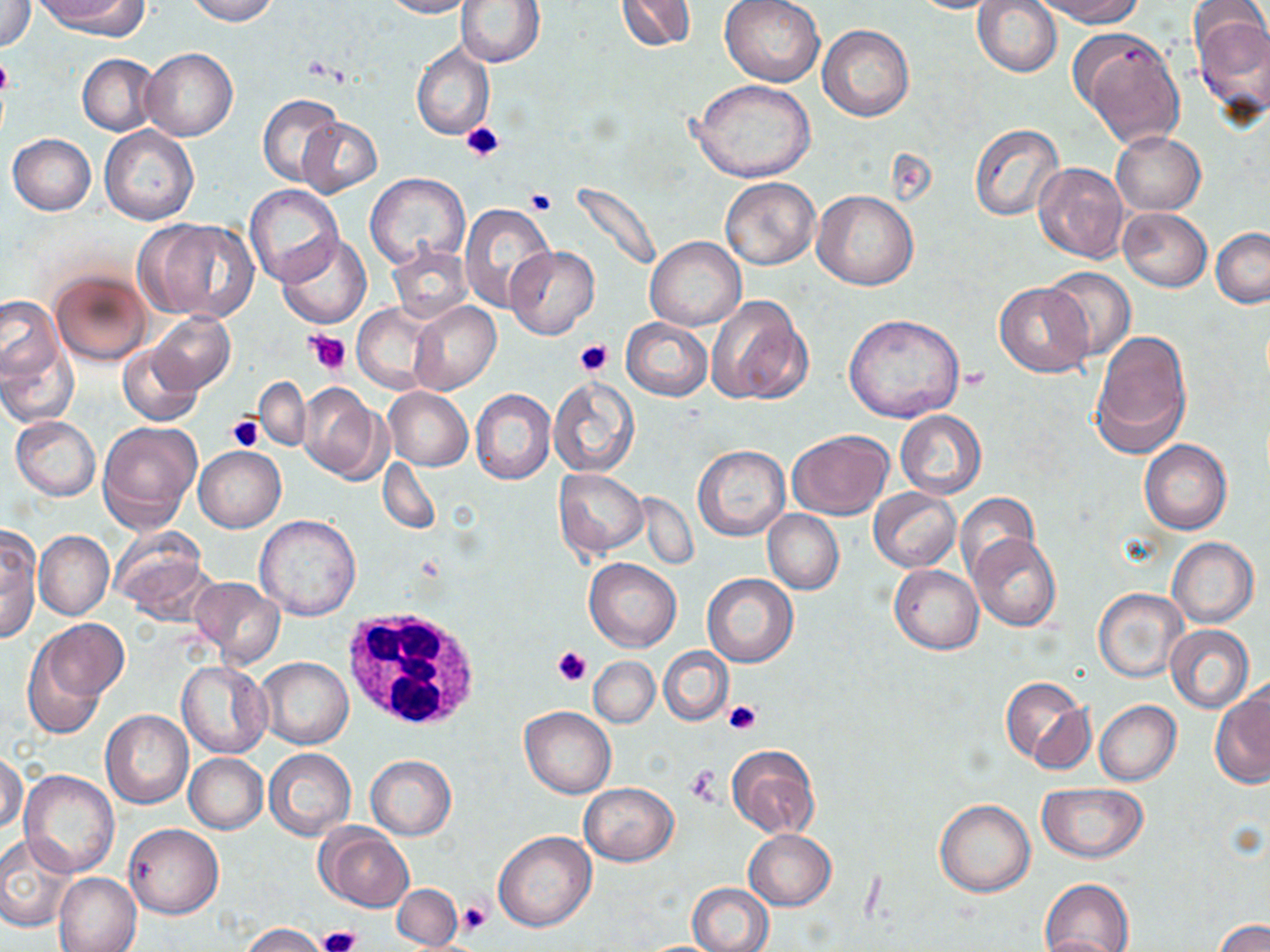 Approximate bounding boxes as [x1, y1, x2, y2] in pixels. Platelet locations: [0, 54, 14, 97], [460, 119, 504, 163], [525, 188, 556, 215], [305, 329, 351, 375], [576, 340, 614, 375], [226, 413, 263, 451], [553, 644, 591, 685], [724, 699, 762, 735], [686, 767, 722, 804], [457, 900, 492, 937], [317, 925, 362, 952]. Uninfected red blood cell locations: [38, 0, 145, 36], [184, 0, 279, 24], [380, 0, 472, 18], [456, 0, 546, 68], [613, 0, 698, 54], [720, 0, 825, 85], [1033, 0, 1144, 26], [1, 1, 36, 51], [905, 1, 1012, 14], [974, 1, 1061, 76], [1195, 15, 1270, 115], [817, 23, 913, 121], [1075, 31, 1186, 149], [412, 43, 494, 139], [139, 48, 237, 140], [78, 55, 159, 134], [690, 79, 818, 184], [259, 95, 346, 187], [296, 117, 382, 197], [968, 122, 1066, 220], [100, 125, 199, 226], [1111, 131, 1205, 215], [7, 134, 96, 216], [1033, 162, 1130, 263], [365, 173, 470, 269], [720, 177, 821, 271], [570, 179, 662, 277], [244, 184, 343, 285], [812, 190, 918, 291], [458, 202, 556, 315], [1118, 208, 1211, 292], [139, 219, 257, 323], [1211, 227, 1270, 307], [276, 234, 373, 329], [644, 236, 746, 330], [387, 244, 475, 324], [506, 246, 599, 340], [51, 267, 152, 365], [1043, 267, 1135, 360], [994, 281, 1093, 378], [0, 294, 68, 401], [704, 295, 812, 405], [409, 301, 500, 395], [353, 304, 436, 393], [149, 312, 235, 392], [843, 313, 965, 422], [622, 317, 713, 401], [1090, 330, 1192, 457], [117, 343, 203, 426], [549, 375, 640, 476], [255, 377, 311, 451], [297, 382, 388, 483], [383, 387, 473, 470], [470, 389, 556, 484], [895, 410, 986, 499], [10, 415, 100, 500], [98, 420, 203, 533], [787, 431, 894, 519], [1139, 439, 1231, 535], [692, 445, 789, 541], [195, 446, 286, 532], [379, 458, 440, 534], [554, 468, 648, 557], [869, 488, 960, 572], [956, 494, 1039, 583], [763, 510, 844, 594], [254, 514, 362, 620], [0, 525, 41, 641], [111, 530, 212, 622], [33, 531, 113, 620], [969, 533, 1061, 631], [1167, 537, 1258, 628], [584, 558, 680, 652], [889, 564, 984, 655], [702, 573, 798, 667], [191, 576, 285, 666], [1092, 588, 1188, 683], [37, 619, 129, 703], [1165, 625, 1253, 714], [22, 640, 113, 739], [659, 648, 732, 725], [257, 657, 352, 749], [589, 657, 659, 728], [177, 660, 271, 758], [1000, 676, 1094, 772], [1211, 690, 1270, 788], [1094, 700, 1181, 786], [519, 707, 615, 798], [101, 710, 193, 809], [726, 745, 820, 838], [264, 749, 356, 841], [1, 751, 25, 833], [185, 753, 268, 832], [365, 754, 456, 841], [20, 769, 119, 876], [578, 782, 678, 865], [1037, 783, 1148, 862], [935, 800, 1034, 897], [124, 823, 224, 919], [317, 825, 413, 912], [744, 829, 836, 909], [493, 831, 595, 932], [0, 836, 77, 933], [54, 872, 142, 951], [1040, 877, 1136, 952], [688, 881, 775, 952], [394, 884, 462, 948], [1216, 919, 1268, 952], [243, 923, 329, 952], [1038, 935, 1126, 952]. White blood cell locations: [338, 605, 488, 735]. Slide-level diagnosis: no evidence of blood parasites. Thin blood smear. Captured at 1000x magnification. Light microscopy. May-Grünwald-Giemsa stain. Image is 1270×952 pixels. Single field of view.